Comment on the morphology of the red blood cells.
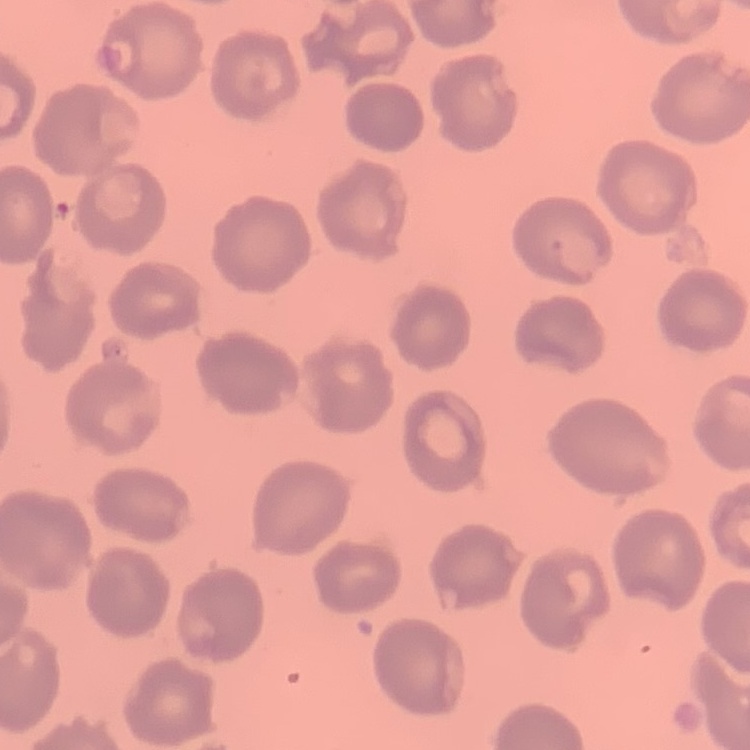
No rouleaux formation.

Summary:
  - Image type: square crop of a larger photomicrograph
  - Stain: Field's or Giemsa
  - Preparation: thin blood smear